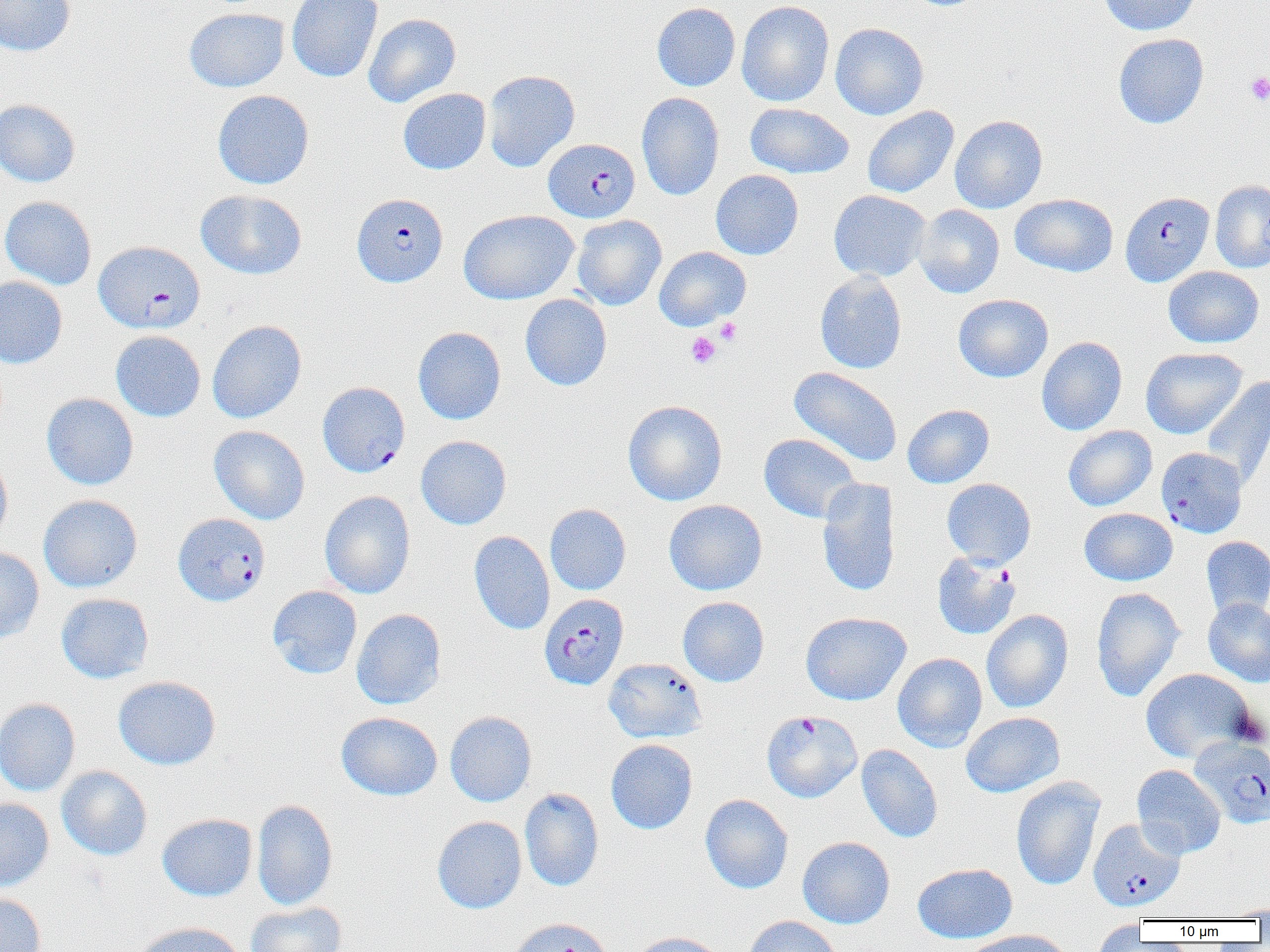

Approximate bounding boxes as named x1/y1/x2/y2 corners in pixels. Plasmodium falciparum-infected red blood cell locations: (x1=544, y1=138, x2=640, y2=222), (x1=1120, y1=191, x2=1214, y2=287), (x1=352, y1=193, x2=448, y2=287), (x1=94, y1=241, x2=205, y2=334), (x1=317, y1=382, x2=410, y2=478), (x1=1155, y1=447, x2=1248, y2=538), (x1=173, y1=513, x2=270, y2=606), (x1=932, y1=552, x2=1021, y2=640), (x1=539, y1=587, x2=629, y2=684), (x1=761, y1=710, x2=862, y2=803), (x1=1190, y1=736, x2=1270, y2=829), (x1=1088, y1=818, x2=1185, y2=911). Platelet locations: (x1=1246, y1=72, x2=1270, y2=105), (x1=714, y1=318, x2=743, y2=345), (x1=686, y1=331, x2=721, y2=368). Uninfected red blood cell locations: (x1=0, y1=0, x2=75, y2=56), (x1=287, y1=0, x2=383, y2=82), (x1=736, y1=0, x2=834, y2=107), (x1=1097, y1=0, x2=1201, y2=36), (x1=651, y1=2, x2=740, y2=91), (x1=184, y1=8, x2=289, y2=92), (x1=363, y1=13, x2=461, y2=107), (x1=830, y1=23, x2=929, y2=120), (x1=1113, y1=33, x2=1209, y2=128), (x1=482, y1=69, x2=580, y2=172), (x1=398, y1=88, x2=491, y2=175), (x1=213, y1=90, x2=314, y2=189), (x1=637, y1=91, x2=724, y2=201), (x1=0, y1=98, x2=81, y2=187), (x1=745, y1=102, x2=854, y2=179), (x1=862, y1=106, x2=959, y2=198), (x1=950, y1=114, x2=1048, y2=213), (x1=710, y1=169, x2=803, y2=260), (x1=1210, y1=179, x2=1270, y2=273), (x1=196, y1=189, x2=307, y2=280), (x1=829, y1=190, x2=931, y2=281), (x1=1010, y1=193, x2=1118, y2=277), (x1=0, y1=196, x2=97, y2=290), (x1=913, y1=205, x2=1004, y2=298), (x1=458, y1=209, x2=579, y2=304), (x1=571, y1=215, x2=667, y2=311), (x1=653, y1=246, x2=751, y2=331), (x1=1163, y1=266, x2=1264, y2=348), (x1=814, y1=271, x2=907, y2=374), (x1=0, y1=276, x2=68, y2=369), (x1=520, y1=294, x2=612, y2=391), (x1=953, y1=294, x2=1053, y2=382), (x1=207, y1=320, x2=307, y2=423), (x1=413, y1=326, x2=506, y2=425), (x1=110, y1=330, x2=206, y2=422), (x1=1037, y1=336, x2=1127, y2=435), (x1=1140, y1=347, x2=1247, y2=439), (x1=788, y1=367, x2=902, y2=467), (x1=1200, y1=375, x2=1270, y2=491), (x1=42, y1=393, x2=139, y2=490), (x1=623, y1=400, x2=727, y2=506), (x1=902, y1=404, x2=994, y2=489), (x1=209, y1=425, x2=310, y2=524), (x1=1063, y1=425, x2=1157, y2=512), (x1=758, y1=433, x2=863, y2=523), (x1=415, y1=435, x2=512, y2=529), (x1=0, y1=450, x2=12, y2=547), (x1=816, y1=478, x2=900, y2=597), (x1=941, y1=478, x2=1036, y2=568), (x1=319, y1=491, x2=416, y2=599), (x1=38, y1=494, x2=143, y2=592), (x1=664, y1=499, x2=768, y2=595), (x1=545, y1=503, x2=631, y2=595), (x1=1079, y1=508, x2=1177, y2=585), (x1=469, y1=530, x2=555, y2=635), (x1=1200, y1=535, x2=1270, y2=619), (x1=0, y1=547, x2=44, y2=642), (x1=267, y1=585, x2=362, y2=679), (x1=1091, y1=586, x2=1186, y2=702), (x1=56, y1=592, x2=154, y2=684), (x1=681, y1=596, x2=773, y2=687), (x1=1203, y1=598, x2=1270, y2=687), (x1=351, y1=608, x2=446, y2=710), (x1=981, y1=609, x2=1073, y2=713), (x1=801, y1=612, x2=911, y2=706), (x1=892, y1=652, x2=987, y2=752), (x1=603, y1=657, x2=707, y2=744), (x1=1140, y1=668, x2=1256, y2=763), (x1=113, y1=676, x2=221, y2=770), (x1=0, y1=698, x2=80, y2=796), (x1=445, y1=710, x2=537, y2=807), (x1=336, y1=712, x2=443, y2=801), (x1=961, y1=712, x2=1065, y2=797), (x1=606, y1=739, x2=698, y2=834), (x1=856, y1=744, x2=943, y2=843), (x1=1131, y1=764, x2=1226, y2=859), (x1=56, y1=766, x2=152, y2=860), (x1=1010, y1=777, x2=1105, y2=891), (x1=519, y1=787, x2=604, y2=892), (x1=700, y1=794, x2=794, y2=894), (x1=0, y1=797, x2=54, y2=893), (x1=252, y1=799, x2=338, y2=910), (x1=156, y1=813, x2=258, y2=901), (x1=432, y1=816, x2=527, y2=914), (x1=797, y1=836, x2=895, y2=928), (x1=912, y1=863, x2=1017, y2=944), (x1=0, y1=892, x2=47, y2=952), (x1=245, y1=901, x2=347, y2=952), (x1=1226, y1=902, x2=1270, y2=920), (x1=743, y1=915, x2=842, y2=952), (x1=507, y1=917, x2=615, y2=952), (x1=1088, y1=920, x2=1148, y2=952), (x1=132, y1=921, x2=246, y2=952), (x1=964, y1=929, x2=1073, y2=952), (x1=628, y1=931, x2=731, y2=952). Slide-level diagnosis: Plasmodium falciparum. Optical microscopy. 1000x magnification. One field of a larger specimen. Image is 1270×952 pixels. Thin blood film.